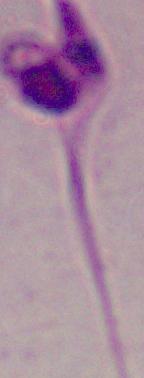

A Leishmania parasite is seen. Micrograph. Captured at 1000x magnification.